Name the parasite shown.
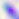
This is Toxoplasma gondii.

Summary:
  - Modality: photomicrograph
  - Magnification: 400x